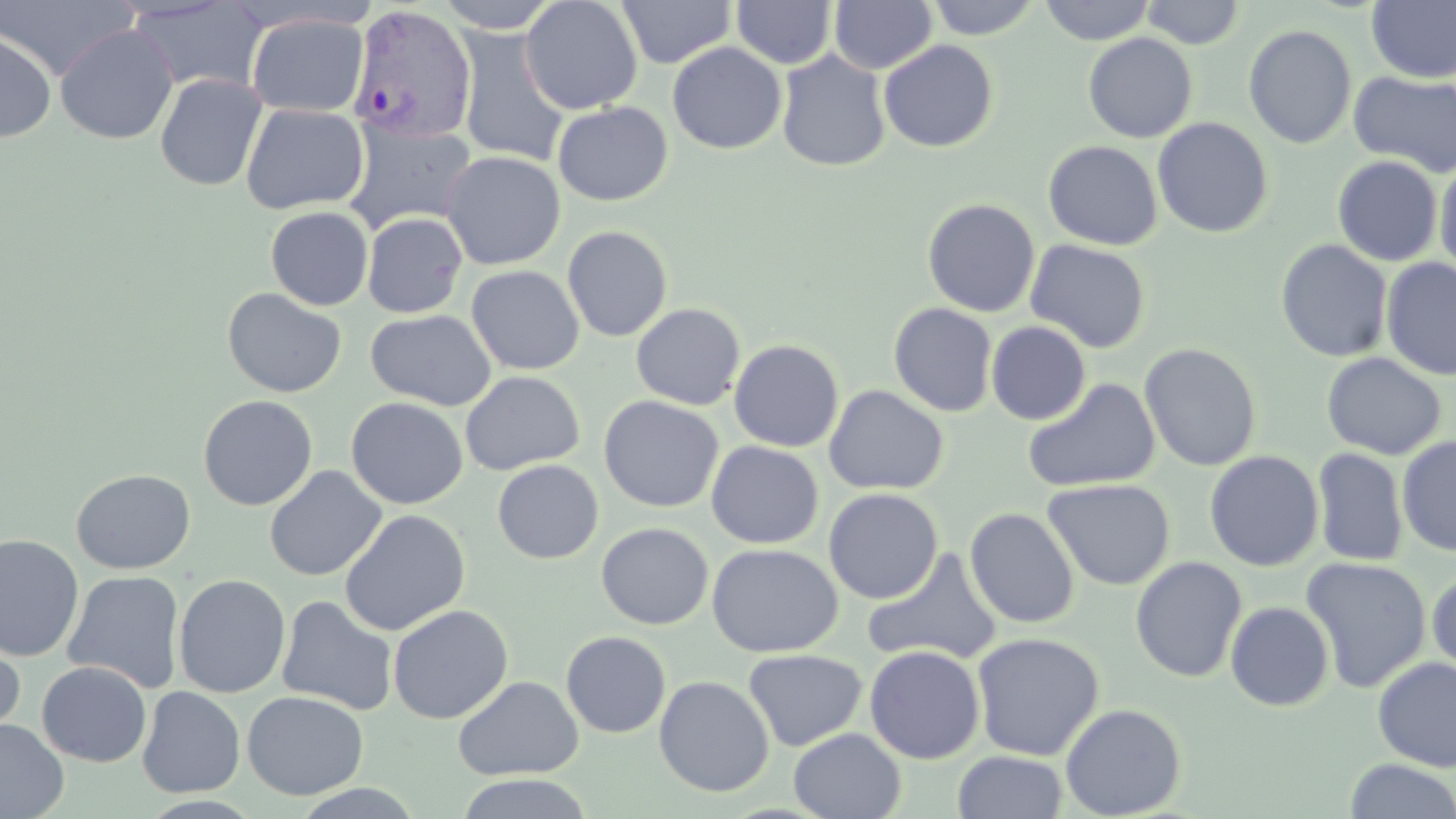

Approximate bounding boxes as named x1/y1/x2/y2 corners in pixels. Plasmodium vivax-infected red blood cell locations: (x1=347, y1=4, x2=477, y2=145). Uninfected red blood cell locations: (x1=0, y1=0, x2=138, y2=80), (x1=434, y1=0, x2=564, y2=33), (x1=520, y1=0, x2=643, y2=115), (x1=616, y1=0, x2=736, y2=68), (x1=829, y1=0, x2=937, y2=74), (x1=926, y1=0, x2=1041, y2=40), (x1=1038, y1=0, x2=1156, y2=46), (x1=126, y1=1, x2=268, y2=94), (x1=731, y1=1, x2=837, y2=69), (x1=1140, y1=1, x2=1246, y2=49), (x1=1366, y1=1, x2=1456, y2=83), (x1=246, y1=13, x2=369, y2=116), (x1=55, y1=24, x2=178, y2=144), (x1=1243, y1=24, x2=1357, y2=149), (x1=455, y1=27, x2=571, y2=168), (x1=0, y1=28, x2=57, y2=143), (x1=1082, y1=33, x2=1198, y2=143), (x1=879, y1=39, x2=999, y2=153), (x1=667, y1=41, x2=787, y2=154), (x1=776, y1=50, x2=891, y2=172), (x1=1348, y1=70, x2=1456, y2=178), (x1=154, y1=73, x2=267, y2=191), (x1=552, y1=101, x2=672, y2=206), (x1=241, y1=103, x2=369, y2=215), (x1=1152, y1=117, x2=1274, y2=239), (x1=344, y1=120, x2=477, y2=236), (x1=1042, y1=140, x2=1163, y2=250), (x1=440, y1=150, x2=566, y2=270), (x1=1332, y1=155, x2=1443, y2=266), (x1=1435, y1=158, x2=1456, y2=279), (x1=921, y1=198, x2=1040, y2=317), (x1=265, y1=206, x2=373, y2=310), (x1=362, y1=212, x2=467, y2=318), (x1=562, y1=225, x2=672, y2=342), (x1=1025, y1=239, x2=1151, y2=354), (x1=1275, y1=239, x2=1392, y2=363), (x1=1381, y1=257, x2=1456, y2=380), (x1=466, y1=265, x2=584, y2=375), (x1=222, y1=287, x2=347, y2=398), (x1=631, y1=303, x2=746, y2=410), (x1=888, y1=303, x2=998, y2=417), (x1=364, y1=309, x2=497, y2=411), (x1=986, y1=321, x2=1091, y2=424), (x1=728, y1=339, x2=844, y2=452), (x1=1139, y1=343, x2=1262, y2=472), (x1=1321, y1=352, x2=1446, y2=460), (x1=460, y1=371, x2=584, y2=476), (x1=1021, y1=378, x2=1161, y2=493), (x1=823, y1=385, x2=949, y2=496), (x1=197, y1=394, x2=318, y2=511), (x1=599, y1=395, x2=724, y2=513), (x1=346, y1=397, x2=468, y2=510), (x1=1397, y1=436, x2=1456, y2=558), (x1=706, y1=441, x2=823, y2=549), (x1=1312, y1=447, x2=1408, y2=567), (x1=1204, y1=450, x2=1324, y2=571), (x1=492, y1=459, x2=604, y2=564), (x1=264, y1=465, x2=386, y2=581), (x1=71, y1=469, x2=196, y2=574), (x1=1042, y1=478, x2=1176, y2=590), (x1=823, y1=488, x2=943, y2=604), (x1=964, y1=507, x2=1080, y2=629), (x1=339, y1=509, x2=470, y2=636), (x1=596, y1=522, x2=713, y2=630), (x1=0, y1=534, x2=84, y2=660), (x1=706, y1=542, x2=843, y2=658), (x1=863, y1=548, x2=1003, y2=666), (x1=1130, y1=556, x2=1248, y2=683), (x1=1300, y1=557, x2=1432, y2=693), (x1=1427, y1=568, x2=1456, y2=677), (x1=63, y1=570, x2=185, y2=694), (x1=173, y1=574, x2=291, y2=699), (x1=276, y1=595, x2=398, y2=716), (x1=1225, y1=601, x2=1335, y2=712), (x1=388, y1=605, x2=514, y2=725), (x1=561, y1=631, x2=671, y2=738), (x1=971, y1=632, x2=1105, y2=761), (x1=0, y1=635, x2=25, y2=746), (x1=864, y1=645, x2=985, y2=764), (x1=743, y1=649, x2=867, y2=751), (x1=1372, y1=656, x2=1456, y2=773), (x1=37, y1=661, x2=152, y2=766), (x1=452, y1=675, x2=584, y2=781), (x1=654, y1=675, x2=774, y2=797), (x1=137, y1=686, x2=246, y2=797), (x1=242, y1=690, x2=369, y2=800), (x1=1060, y1=703, x2=1187, y2=818), (x1=0, y1=718, x2=69, y2=819), (x1=788, y1=728, x2=906, y2=818), (x1=952, y1=750, x2=1068, y2=819), (x1=1343, y1=758, x2=1456, y2=818), (x1=453, y1=773, x2=595, y2=818), (x1=287, y1=783, x2=427, y2=818). Slide-level diagnosis: Plasmodium vivax. Thin blood smear. May-Grünwald-Giemsa stain. Single field of view. Image is 1456×819 pixels. Light microscopy. 1000x magnification.